Identify the parasite.
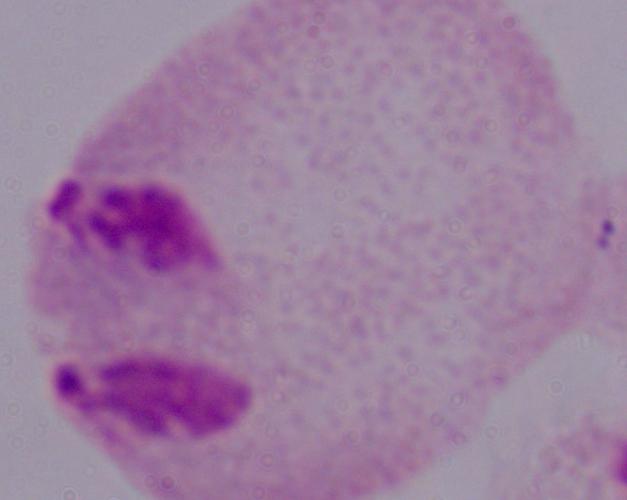

This is a trichomonad.

Captured at 1000x magnification. Photomicrograph.